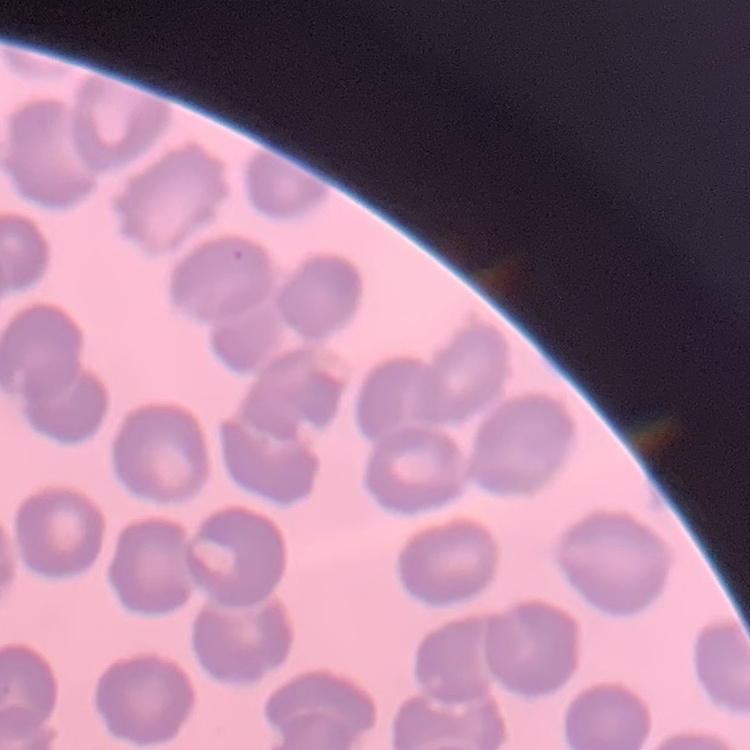 The erythrocytes exhibit no rouleaux formation. Square crop of a larger photomicrograph. Thin blood smear. Field's or Giemsa stain.